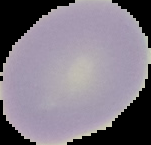
image_type: segmented cell region with the area outside set to black
image_size: 151×145 pixels
preparation: thin blood smear
malaria_status: uninfected